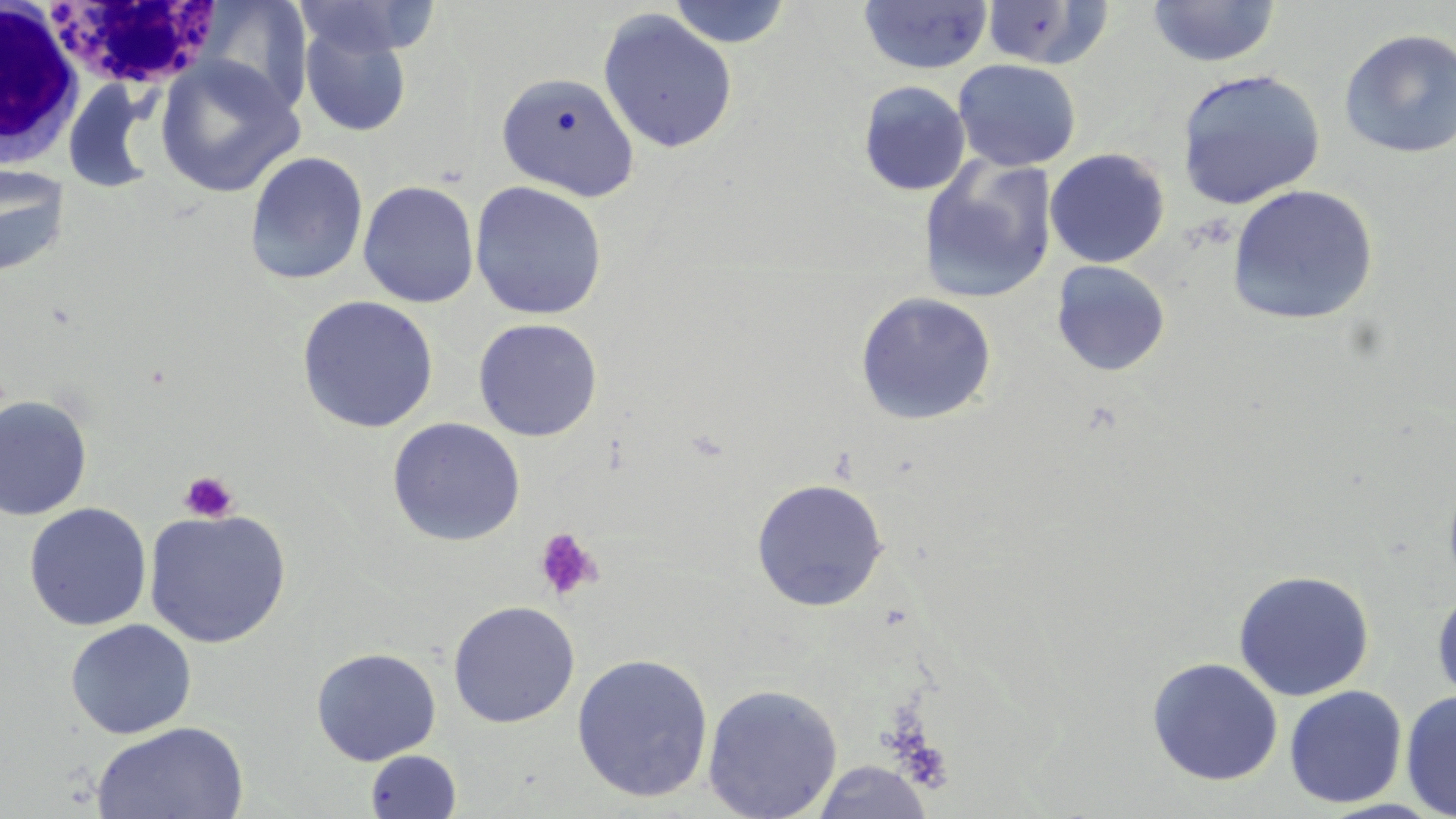
{
  "slide_level_diagnosis": "negative for blood parasites",
  "field_of_view": "one of a larger specimen",
  "white_blood_cell_locations": "approximate bounding boxes as named x1/y1/x2/y2 corners in pixels: (x1=45, y1=2, x2=227, y2=91), (x1=0, y1=3, x2=84, y2=169)",
  "preparation": "thin blood smear",
  "platelet_locations": "approximate bounding boxes as named x1/y1/x2/y2 corners in pixels: (x1=179, y1=471, x2=239, y2=522), (x1=533, y1=528, x2=602, y2=601), (x1=885, y1=728, x2=956, y2=794)",
  "uninfected_red_blood_cell_locations": "approximate bounding boxes as named x1/y1/x2/y2 corners in pixels: (x1=291, y1=0, x2=439, y2=59), (x1=198, y1=1, x2=313, y2=114), (x1=666, y1=1, x2=794, y2=49), (x1=858, y1=1, x2=993, y2=74), (x1=1146, y1=1, x2=1281, y2=68), (x1=979, y1=2, x2=1115, y2=70), (x1=1, y1=7, x2=85, y2=234), (x1=597, y1=9, x2=738, y2=154), (x1=299, y1=20, x2=414, y2=138), (x1=1339, y1=28, x2=1456, y2=159), (x1=154, y1=55, x2=305, y2=199), (x1=952, y1=58, x2=1082, y2=172), (x1=1175, y1=69, x2=1326, y2=211), (x1=495, y1=72, x2=639, y2=201), (x1=62, y1=79, x2=156, y2=193), (x1=858, y1=81, x2=970, y2=196), (x1=1045, y1=148, x2=1169, y2=268), (x1=243, y1=151, x2=368, y2=286), (x1=917, y1=155, x2=1059, y2=305), (x1=0, y1=162, x2=72, y2=277), (x1=357, y1=180, x2=479, y2=308), (x1=470, y1=180, x2=608, y2=321), (x1=1227, y1=184, x2=1379, y2=326), (x1=1051, y1=260, x2=1171, y2=377), (x1=855, y1=291, x2=997, y2=426), (x1=297, y1=295, x2=439, y2=434), (x1=473, y1=318, x2=603, y2=441), (x1=0, y1=394, x2=93, y2=521), (x1=386, y1=417, x2=525, y2=546), (x1=750, y1=477, x2=889, y2=612), (x1=24, y1=503, x2=152, y2=632), (x1=143, y1=509, x2=291, y2=648), (x1=1233, y1=569, x2=1375, y2=701), (x1=1431, y1=585, x2=1456, y2=707), (x1=447, y1=600, x2=580, y2=728), (x1=64, y1=619, x2=197, y2=739), (x1=310, y1=646, x2=442, y2=766), (x1=571, y1=652, x2=714, y2=803), (x1=1146, y1=657, x2=1284, y2=786), (x1=701, y1=683, x2=843, y2=819), (x1=1283, y1=685, x2=1407, y2=808), (x1=1400, y1=690, x2=1456, y2=818), (x1=93, y1=720, x2=249, y2=819), (x1=365, y1=749, x2=462, y2=818), (x1=811, y1=761, x2=932, y2=819)",
  "stain": "May-Grünwald-Giemsa",
  "modality": "light microscopy",
  "image_size": "1456×819 pixels",
  "magnification": "1000x"
}